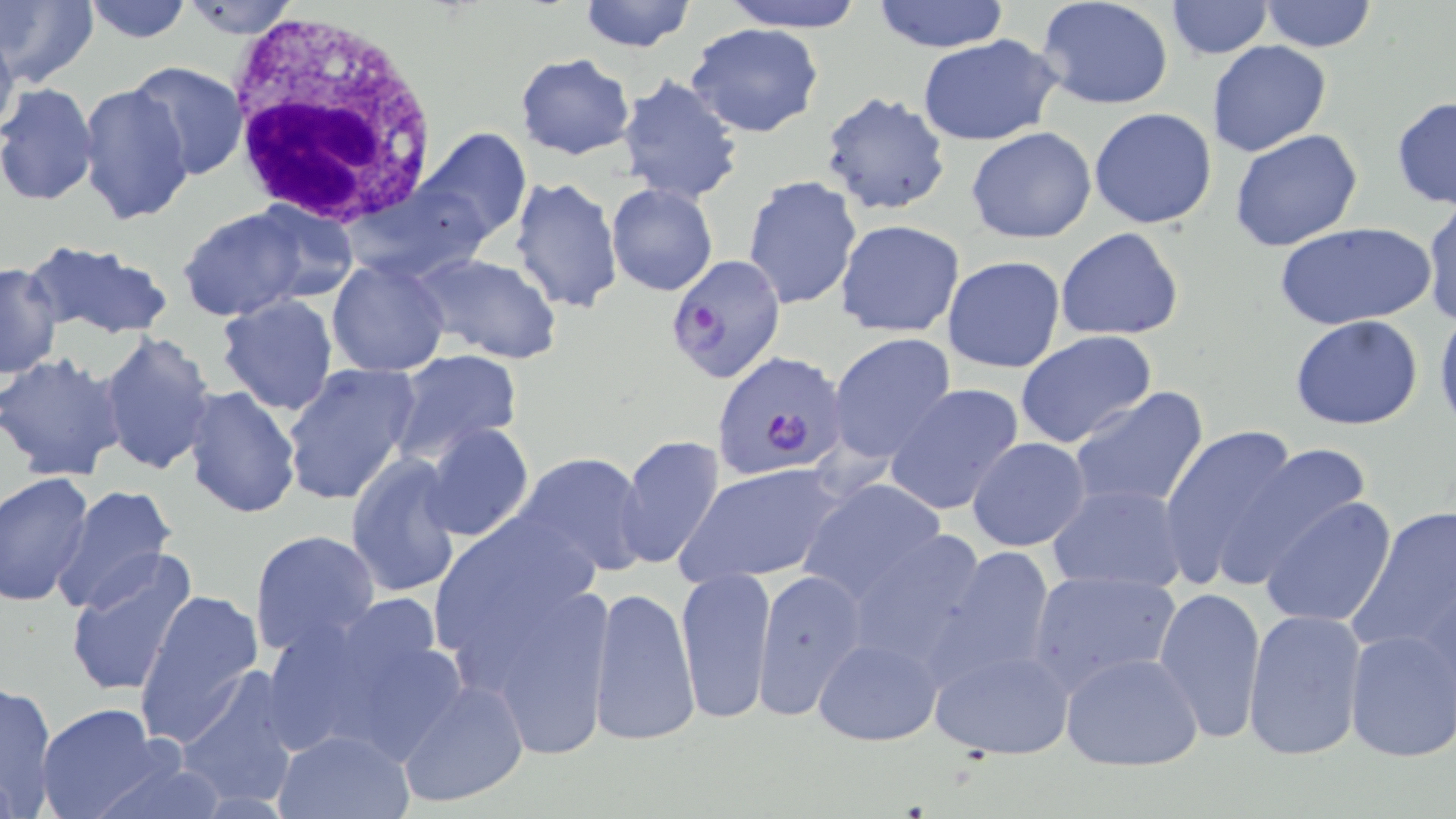
Summary:
  - Coordinate format: approximate bounding boxes as (x1,y1)-(x2,y2) corner pairs in pixels
  - Uninfected red blood cell locations: (0,0)-(98,87), (178,0)-(301,39), (576,0)-(698,53), (718,0)-(868,33), (869,0)-(1011,52), (1258,0)-(1379,53), (81,1)-(194,45), (1037,1)-(1174,110), (1166,1)-(1272,58), (0,20)-(19,144), (686,22)-(825,137), (916,33)-(1066,146), (1207,41)-(1332,157), (515,52)-(636,160), (129,60)-(250,181), (617,73)-(744,204), (0,82)-(100,208), (78,83)-(193,228), (819,91)-(952,215), (1391,95)-(1456,212), (1089,108)-(1218,229), (965,127)-(1096,244), (1229,127)-(1363,252), (415,129)-(530,245), (742,174)-(862,310), (510,175)-(623,316), (606,181)-(718,297), (1421,194)-(1456,332), (249,199)-(357,303), (177,207)-(310,321), (835,219)-(964,338), (1276,220)-(1435,332), (1056,228)-(1185,342), (22,240)-(176,342), (416,253)-(562,365), (942,254)-(1066,375), (327,257)-(451,376), (1,261)-(62,379), (215,294)-(339,416), (1434,304)-(1456,436), (1289,315)-(1424,430), (98,331)-(217,477), (1015,331)-(1157,449), (828,334)-(958,466), (387,350)-(524,465), (0,353)-(127,481), (280,364)-(421,506), (883,383)-(1024,515), (182,385)-(302,520), (1068,386)-(1210,515), (421,421)-(535,543), (1158,424)-(1310,595), (361,431)-(517,569), (616,434)-(726,572), (967,437)-(1090,553), (1224,442)-(1376,573), (515,452)-(652,576), (347,453)-(464,599), (675,462)-(848,587), (0,473)-(97,606), (800,478)-(950,606), (1045,483)-(1189,597), (51,484)-(181,618), (1259,495)-(1399,631), (1347,502)-(1455,664), (428,510)-(601,689), (839,527)-(992,674), (249,529)-(380,655), (932,543)-(1058,687), (65,551)-(198,699), (676,565)-(777,727), (1026,568)-(1182,695), (752,569)-(868,719), (460,577)-(620,763), (590,583)-(699,745), (1153,585)-(1267,744), (135,588)-(265,748), (261,598)-(461,765), (1242,609)-(1368,763), (1341,626)-(1456,764), (812,636)-(943,746), (931,643)-(1075,762), (1060,650)-(1206,772), (176,668)-(303,809), (394,676)-(531,810), (0,679)-(58,817), (36,703)-(167,818), (276,728)-(412,817), (85,750)-(229,819)
  - White blood cell locations: (225,12)-(437,231)
  - Plasmodium falciparum-infected red blood cell locations: (663,256)-(785,385), (713,351)-(850,482)
  - Slide-level diagnosis: Plasmodium falciparum
  - Magnification: 1000x
  - Modality: light microscopy
  - Preparation: thin blood smear
  - Stain: May-Grünwald-Giemsa
  - Field of view: single
  - Image size: 1456×819 pixels